Assess the morphology of the erythrocytes.
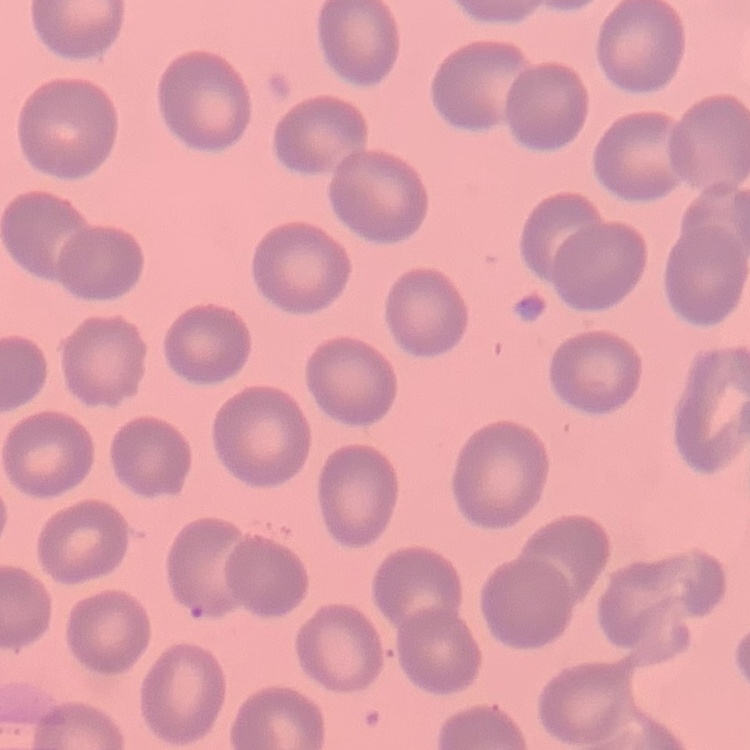

They show no rouleaux formation.

preparation = thin blood smear
image type = square crop of a larger photomicrograph
stain = Field's or Giemsa